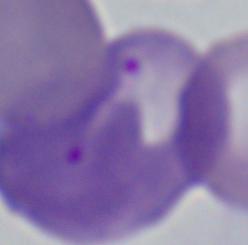

Summary:
  - Identification: Babesia
  - Modality: micrograph
  - Magnification: 1000x